Report the malaria status of this cell.
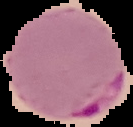

Parasitized.

image_size: 133×127 pixels
preparation: thin blood film
image_type: segmented cell region with the area outside set to black